Outline each blood parasite and name the species.
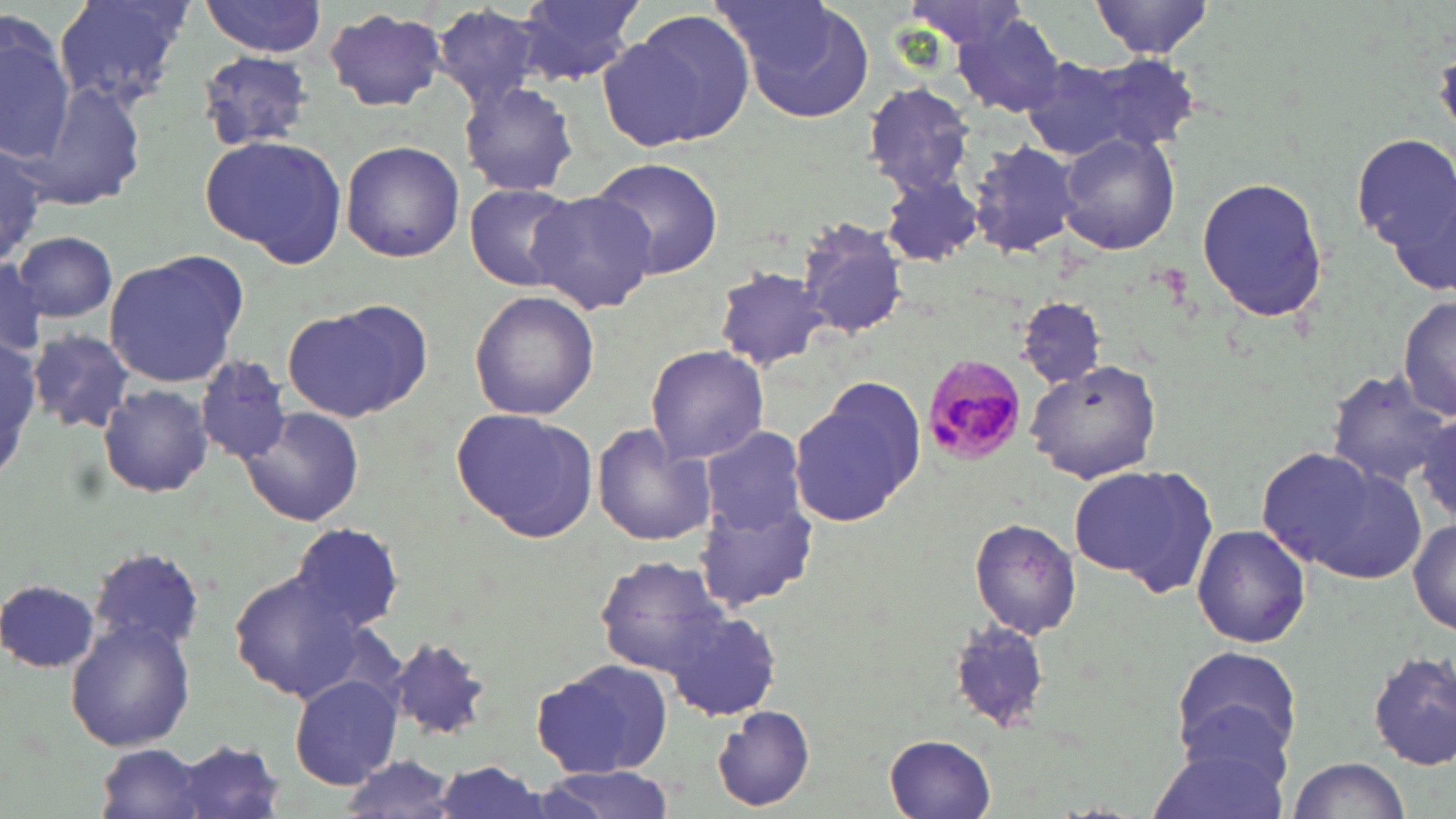

Approximate bounding boxes as [x1, y1, x2, y2] in pixels.
Plasmodium malariae-infected red blood cells: [921, 354, 1031, 466].
No Plasmodium falciparum, Plasmodium ovale, Plasmodium vivax, Babesia divergens, or Trypanosoma brucei observed.

Uninfected red blood cell locations: [55, 0, 192, 112], [200, 0, 329, 56], [515, 0, 649, 83], [720, 0, 877, 125], [898, 0, 1039, 58], [1090, 0, 1215, 57], [432, 4, 548, 112], [324, 8, 448, 113], [606, 10, 757, 151], [0, 12, 75, 161], [954, 14, 1068, 118], [196, 50, 319, 152], [1024, 54, 1193, 163], [861, 80, 977, 197], [25, 81, 147, 210], [458, 81, 580, 198], [1057, 130, 1180, 255], [1355, 132, 1456, 286], [199, 133, 348, 268], [967, 138, 1085, 260], [340, 139, 466, 262], [0, 142, 50, 265], [588, 157, 725, 280], [877, 171, 984, 266], [1196, 174, 1333, 323], [466, 183, 582, 290], [527, 190, 658, 315], [796, 217, 911, 341], [14, 230, 117, 320], [104, 254, 245, 388], [0, 259, 48, 358], [712, 263, 836, 374], [469, 290, 598, 422], [1397, 296, 1455, 423], [1017, 297, 1104, 390], [282, 301, 428, 422], [30, 329, 134, 436], [0, 339, 46, 473], [645, 344, 771, 463], [195, 355, 291, 463], [1027, 359, 1163, 482], [1327, 370, 1451, 489], [789, 377, 925, 525], [97, 382, 214, 498], [453, 405, 597, 541], [239, 407, 366, 528], [1413, 413, 1455, 529], [591, 425, 717, 548], [701, 429, 811, 535], [1257, 445, 1413, 581], [1068, 465, 1215, 592], [696, 496, 817, 611], [1410, 515, 1456, 634], [971, 519, 1082, 640], [288, 522, 406, 636], [1191, 524, 1313, 647], [90, 547, 207, 649], [598, 555, 733, 676], [229, 568, 367, 701], [3, 579, 101, 674], [665, 611, 786, 720], [947, 618, 1053, 731], [65, 619, 196, 751], [390, 636, 497, 742], [1171, 647, 1302, 767], [1369, 650, 1455, 771], [532, 659, 671, 779], [289, 675, 403, 790], [712, 706, 814, 813], [1148, 728, 1294, 819], [885, 733, 998, 818], [170, 739, 286, 818], [96, 742, 214, 819], [334, 754, 467, 817], [1281, 757, 1412, 819], [422, 759, 556, 819], [534, 766, 680, 819]. Slide-level diagnosis: Plasmodium malariae. 1000x magnification. Light microscopy. Thin blood film. May-Grünwald-Giemsa-stained preparation. Single field of view. Image is 1456×819 pixels.